State which parasite is depicted.
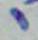

This is Toxoplasma gondii.

Photomicrograph. Captured at 1000x magnification.